Name the parasite shown.
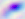
This is Toxoplasma gondii.

Captured at 400x magnification. Micrograph.